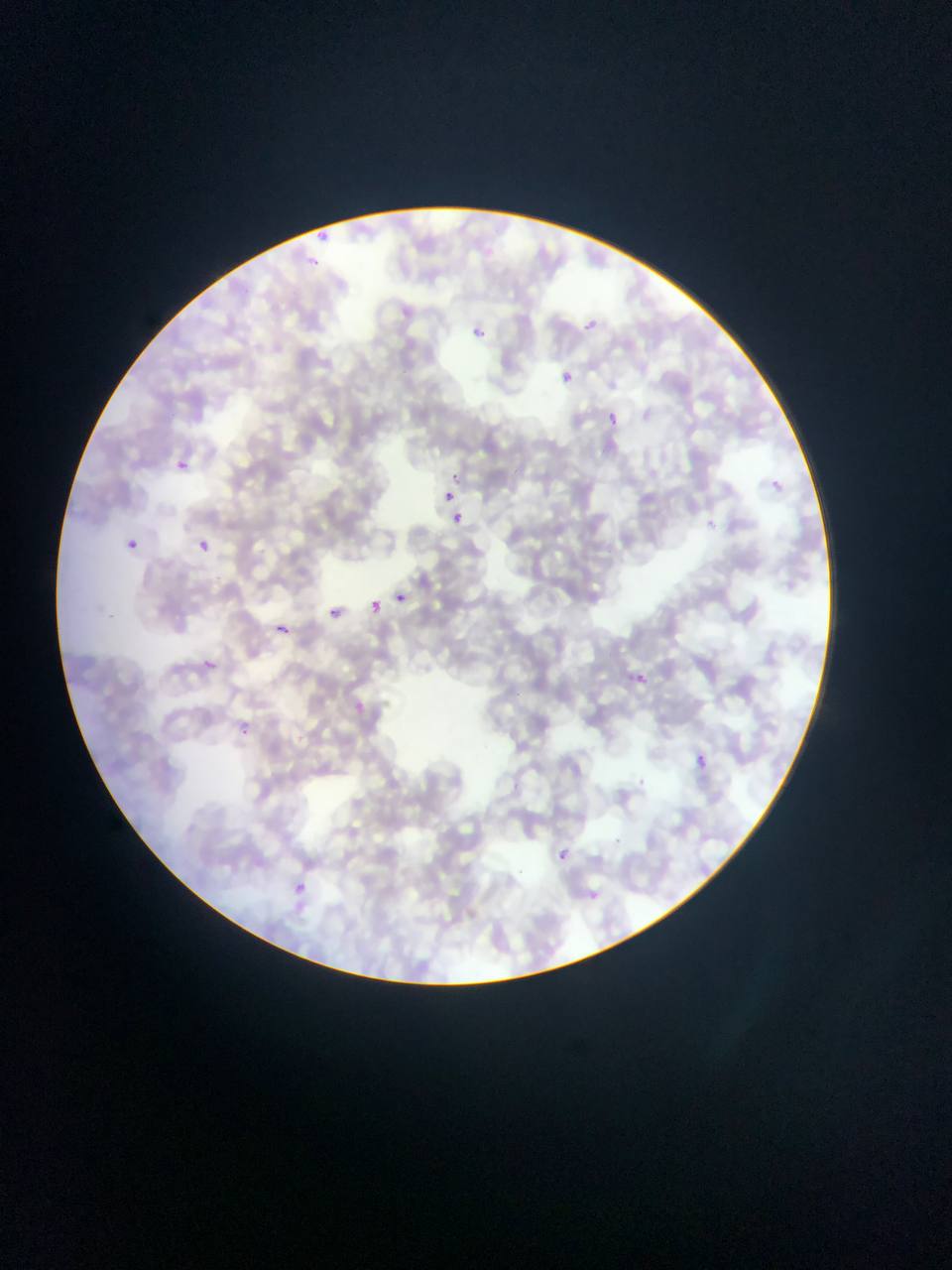
Approximate bounding boxes as {left, top, right, bottom} in pixels. Malaria parasite locations: {315, 230, 325, 242}, {309, 252, 323, 269}, {584, 320, 600, 332}, {475, 323, 494, 346}, {559, 369, 575, 385}, {605, 412, 620, 428}, {169, 455, 195, 478}, {449, 471, 458, 482}, {768, 478, 790, 496}, {442, 490, 455, 503}, {450, 511, 465, 525}, {708, 518, 722, 534}, {123, 538, 138, 552}, {196, 539, 210, 553}, {394, 592, 407, 604}, {369, 600, 382, 613}, {326, 607, 340, 619}, {272, 621, 292, 640}, {201, 656, 221, 680}, {634, 671, 652, 684}, {353, 701, 368, 714}, {239, 718, 251, 739}, {692, 751, 710, 769}, {550, 843, 576, 869}, {282, 874, 316, 906}, {590, 888, 599, 905}. Thin blood smear. Image is 952×1270 pixels. Sample from Ghana. One field of view. Mobile-phone photograph taken through the microscope.